Outline each blood parasite and name the species.
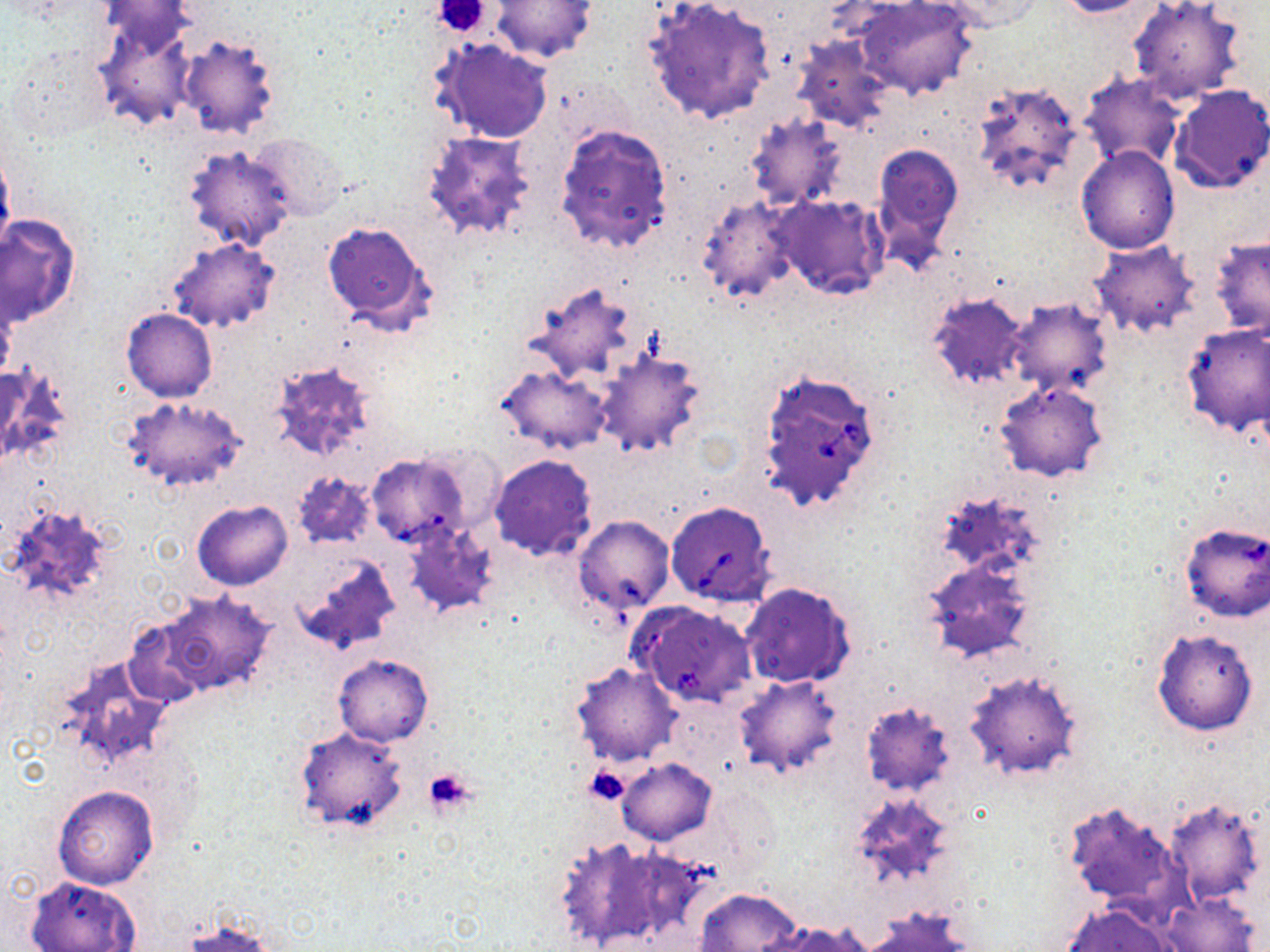
Approximate bounding boxes as named x1/y1/x2/y2 corners in pixels.
Babesia divergens-infected red blood cells: (x1=756, y1=368, x2=884, y2=513), (x1=364, y1=453, x2=476, y2=551), (x1=664, y1=500, x2=776, y2=607).
No Plasmodium falciparum, Plasmodium ovale, Plasmodium malariae, Plasmodium vivax, or Trypanosoma brucei observed.

{
  "slide_level_diagnosis": "Babesia divergens",
  "preparation": "thin blood smear",
  "image_size": "1270×952 pixels",
  "magnification": "1000x",
  "stain": "May-Grünwald-Giemsa",
  "uninfected_red_blood_cell_locations": "approximate bounding boxes as named x1/y1/x2/y2 corners in pixels: (x1=492, y1=0, x2=598, y2=64), (x1=643, y1=0, x2=777, y2=126), (x1=853, y1=0, x2=980, y2=101), (x1=931, y1=0, x2=1042, y2=33), (x1=1052, y1=0, x2=1161, y2=18), (x1=1126, y1=0, x2=1246, y2=107), (x1=92, y1=13, x2=200, y2=132), (x1=793, y1=34, x2=898, y2=135), (x1=176, y1=35, x2=283, y2=139), (x1=429, y1=38, x2=554, y2=145), (x1=5, y1=45, x2=110, y2=143), (x1=1077, y1=75, x2=1186, y2=172), (x1=966, y1=79, x2=1086, y2=199), (x1=1167, y1=84, x2=1269, y2=194), (x1=744, y1=114, x2=851, y2=213), (x1=554, y1=123, x2=673, y2=255), (x1=419, y1=128, x2=540, y2=246), (x1=247, y1=134, x2=345, y2=218), (x1=0, y1=142, x2=15, y2=257), (x1=871, y1=143, x2=963, y2=264), (x1=182, y1=145, x2=297, y2=252), (x1=1076, y1=145, x2=1181, y2=253), (x1=695, y1=192, x2=803, y2=304), (x1=774, y1=195, x2=889, y2=300), (x1=1, y1=215, x2=81, y2=326), (x1=323, y1=223, x2=435, y2=334), (x1=1207, y1=234, x2=1270, y2=339), (x1=168, y1=239, x2=280, y2=333), (x1=1090, y1=241, x2=1201, y2=340), (x1=522, y1=279, x2=641, y2=383), (x1=926, y1=290, x2=1030, y2=393), (x1=0, y1=296, x2=18, y2=383), (x1=1002, y1=298, x2=1114, y2=401), (x1=122, y1=309, x2=217, y2=402), (x1=1181, y1=324, x2=1269, y2=437), (x1=594, y1=347, x2=708, y2=458), (x1=266, y1=361, x2=380, y2=464), (x1=0, y1=365, x2=74, y2=469), (x1=496, y1=365, x2=613, y2=454), (x1=995, y1=381, x2=1109, y2=482), (x1=121, y1=395, x2=248, y2=494), (x1=488, y1=454, x2=598, y2=561), (x1=290, y1=470, x2=377, y2=551), (x1=3, y1=500, x2=117, y2=611), (x1=191, y1=500, x2=293, y2=591), (x1=573, y1=515, x2=675, y2=616), (x1=401, y1=521, x2=500, y2=618), (x1=292, y1=554, x2=402, y2=656), (x1=919, y1=555, x2=1037, y2=664), (x1=740, y1=581, x2=857, y2=689), (x1=148, y1=589, x2=280, y2=701), (x1=1151, y1=629, x2=1258, y2=737), (x1=333, y1=653, x2=433, y2=747), (x1=56, y1=656, x2=175, y2=772), (x1=569, y1=662, x2=683, y2=767), (x1=963, y1=669, x2=1086, y2=781), (x1=733, y1=675, x2=844, y2=779), (x1=859, y1=699, x2=956, y2=798), (x1=293, y1=725, x2=408, y2=835), (x1=616, y1=758, x2=716, y2=845), (x1=705, y1=782, x2=783, y2=877), (x1=52, y1=785, x2=158, y2=888), (x1=843, y1=792, x2=957, y2=892), (x1=1162, y1=798, x2=1266, y2=907), (x1=1062, y1=799, x2=1190, y2=919), (x1=551, y1=835, x2=698, y2=949), (x1=25, y1=876, x2=141, y2=952), (x1=694, y1=888, x2=803, y2=952), (x1=1158, y1=892, x2=1261, y2=952), (x1=1060, y1=903, x2=1180, y2=952), (x1=865, y1=909, x2=973, y2=952), (x1=178, y1=917, x2=277, y2=951), (x1=763, y1=920, x2=872, y2=952)",
  "field_of_view": "single",
  "modality": "light microscopy",
  "platelet_locations": "approximate bounding boxes as named x1/y1/x2/y2 corners in pixels: (x1=430, y1=0, x2=493, y2=38), (x1=421, y1=767, x2=476, y2=818), (x1=584, y1=767, x2=632, y2=805)"
}